Give the position of every leukocyte.
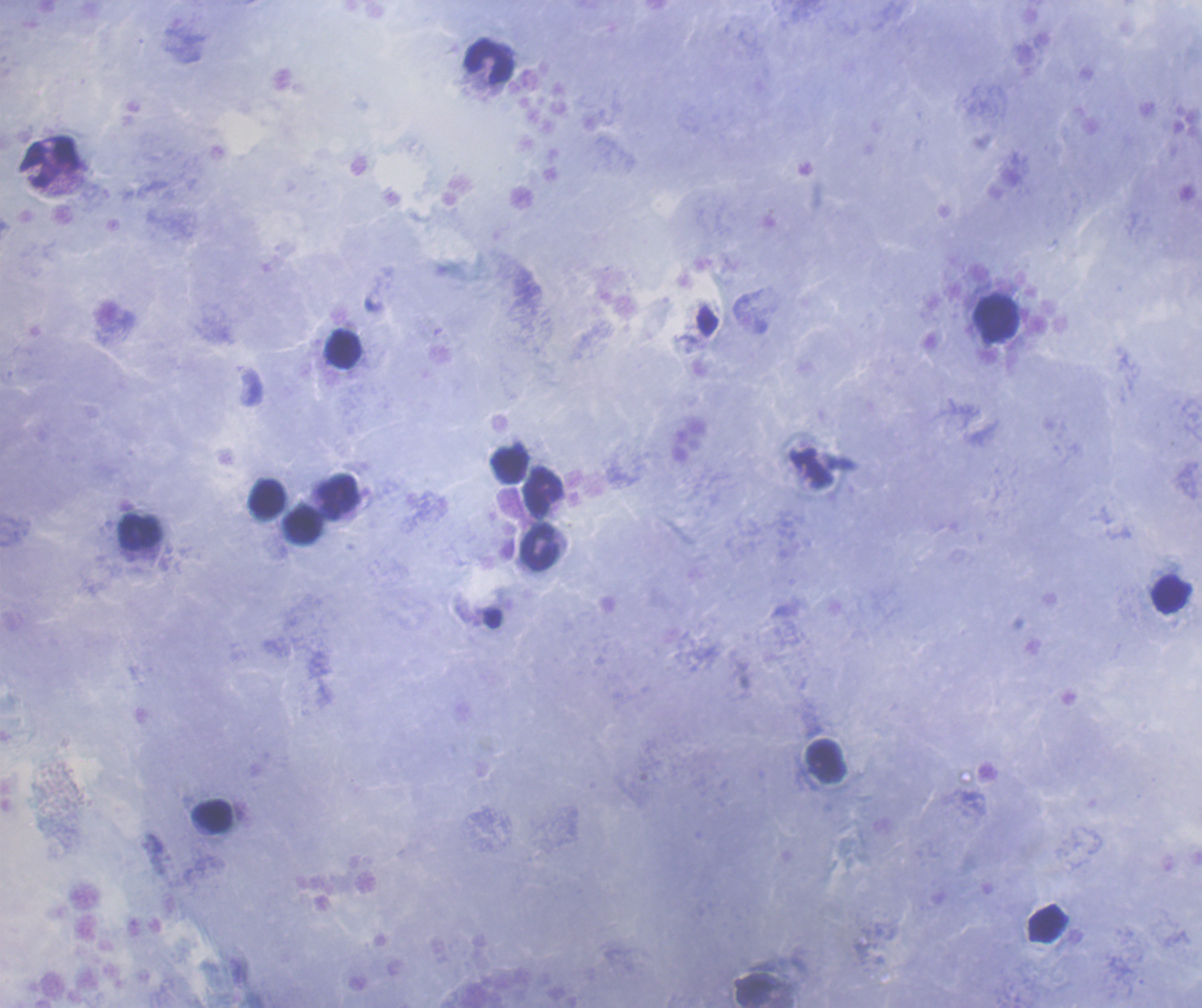
Approximate centers as [x, y] in pixels.
Leukocytes: [491, 62], [49, 161], [997, 319], [344, 349], [510, 465], [544, 492], [336, 497], [267, 500], [304, 526], [141, 533], [540, 549], [1171, 595], [826, 761], [211, 815], [1047, 924], [758, 992].

Summary:
  - Background quality: good
  - Preparation: thick smear of blood
  - Context: previously used in a real diagnosis
  - Coloration quality: good
  - Image size: 1202×1008 pixels
  - Stain: Romanowsky
  - Field of view: one from this slide
  - Magnification: 100x
  - Result: negative for malaria parasites